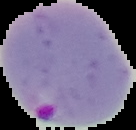 Malaria status: parasitized. The area outside the segmented cell region is set to black. Image is 136×130 pixels. From a thin blood film.